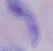

identification = trypanosome
magnification = 1000x
modality = micrograph